Assess the morphology of the erythrocytes.
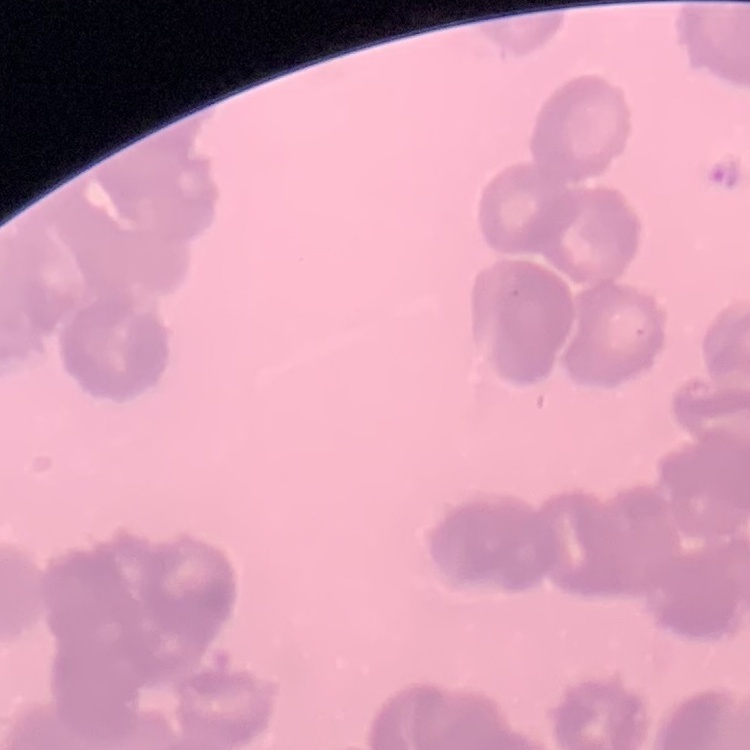

They show rouleaux formation.

image type = one tile cut from a larger photomicrograph
preparation = thin blood film
stain = Field's or Giemsa